Outline each blood parasite and name the species.
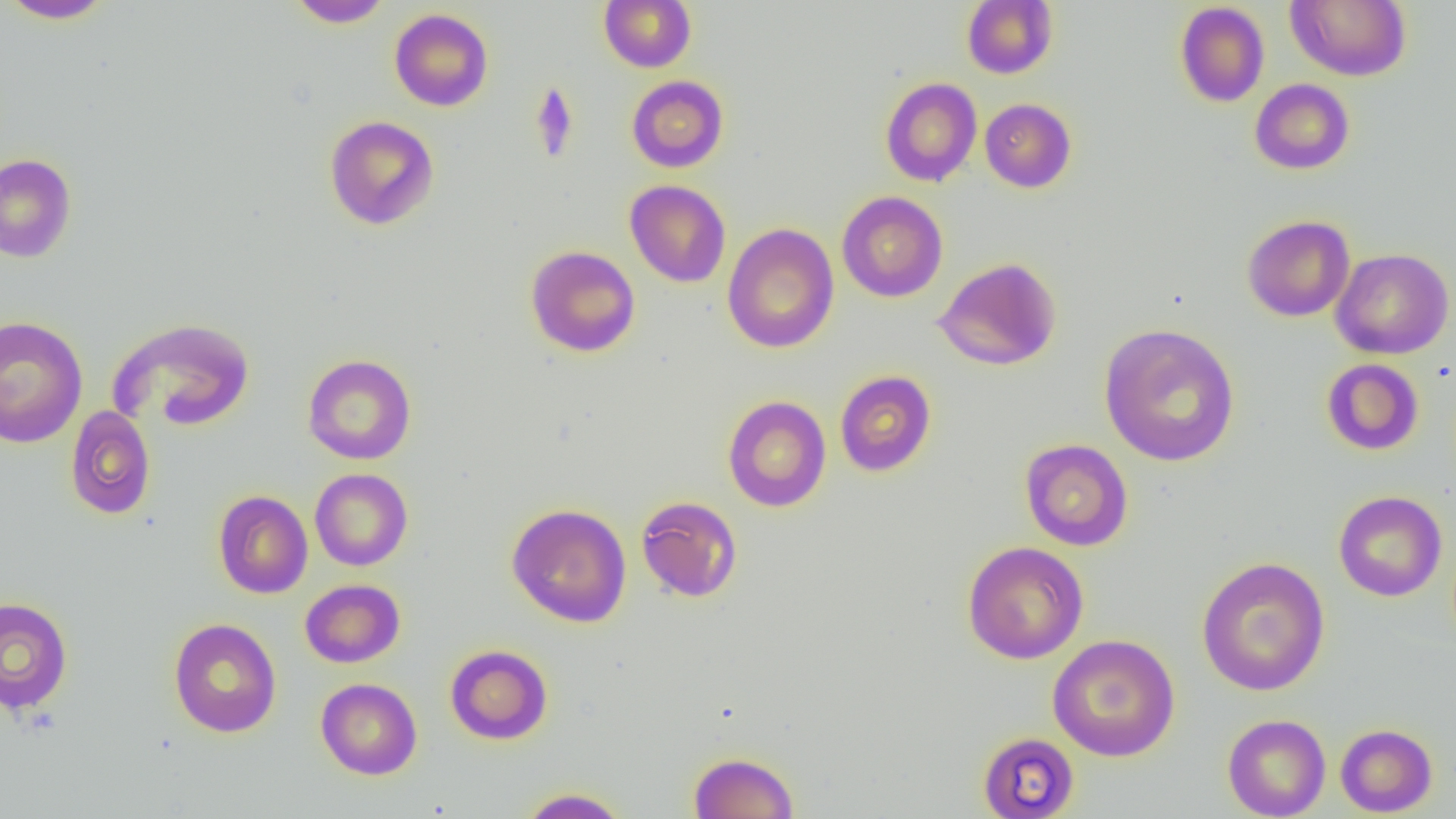
No blood parasites observed.

Summary:
  - Coordinate format: approximate bounding boxes as named x1/y1/x2/y2 corners in pixels
  - Uninfected red blood cell locations: (x1=1, y1=0, x2=116, y2=24), (x1=287, y1=0, x2=393, y2=28), (x1=599, y1=0, x2=696, y2=73), (x1=961, y1=0, x2=1058, y2=79), (x1=1285, y1=0, x2=1412, y2=81), (x1=1174, y1=2, x2=1270, y2=107), (x1=389, y1=8, x2=494, y2=111), (x1=626, y1=74, x2=728, y2=173), (x1=880, y1=77, x2=982, y2=187), (x1=1250, y1=78, x2=1355, y2=174), (x1=979, y1=98, x2=1077, y2=193), (x1=324, y1=115, x2=440, y2=231), (x1=0, y1=153, x2=77, y2=263), (x1=624, y1=180, x2=731, y2=287), (x1=836, y1=190, x2=948, y2=302), (x1=1242, y1=215, x2=1355, y2=322), (x1=722, y1=223, x2=839, y2=354), (x1=525, y1=245, x2=641, y2=356), (x1=1330, y1=248, x2=1454, y2=359), (x1=934, y1=257, x2=1062, y2=371), (x1=0, y1=316, x2=88, y2=449), (x1=108, y1=317, x2=256, y2=433), (x1=1098, y1=323, x2=1240, y2=467), (x1=302, y1=354, x2=417, y2=465), (x1=1321, y1=359, x2=1424, y2=456), (x1=834, y1=370, x2=937, y2=477), (x1=722, y1=395, x2=831, y2=512), (x1=64, y1=405, x2=156, y2=520), (x1=1020, y1=438, x2=1133, y2=551), (x1=310, y1=468, x2=413, y2=571), (x1=212, y1=490, x2=313, y2=599), (x1=1333, y1=491, x2=1448, y2=602), (x1=635, y1=495, x2=743, y2=603), (x1=506, y1=502, x2=632, y2=628), (x1=962, y1=541, x2=1089, y2=664), (x1=1196, y1=556, x2=1330, y2=696), (x1=299, y1=579, x2=405, y2=668), (x1=0, y1=596, x2=74, y2=715), (x1=168, y1=618, x2=282, y2=738), (x1=1047, y1=634, x2=1181, y2=761), (x1=445, y1=644, x2=552, y2=745), (x1=315, y1=677, x2=422, y2=780), (x1=1222, y1=714, x2=1331, y2=818), (x1=1335, y1=723, x2=1438, y2=816), (x1=977, y1=731, x2=1080, y2=818), (x1=689, y1=751, x2=799, y2=818), (x1=517, y1=787, x2=631, y2=818)
  - Slide-level diagnosis: negative for blood parasites
  - Magnification: 1000x
  - Field of view: one of a larger specimen
  - Image size: 1456×819 pixels
  - Modality: optical microscopy
  - Preparation: thin blood film